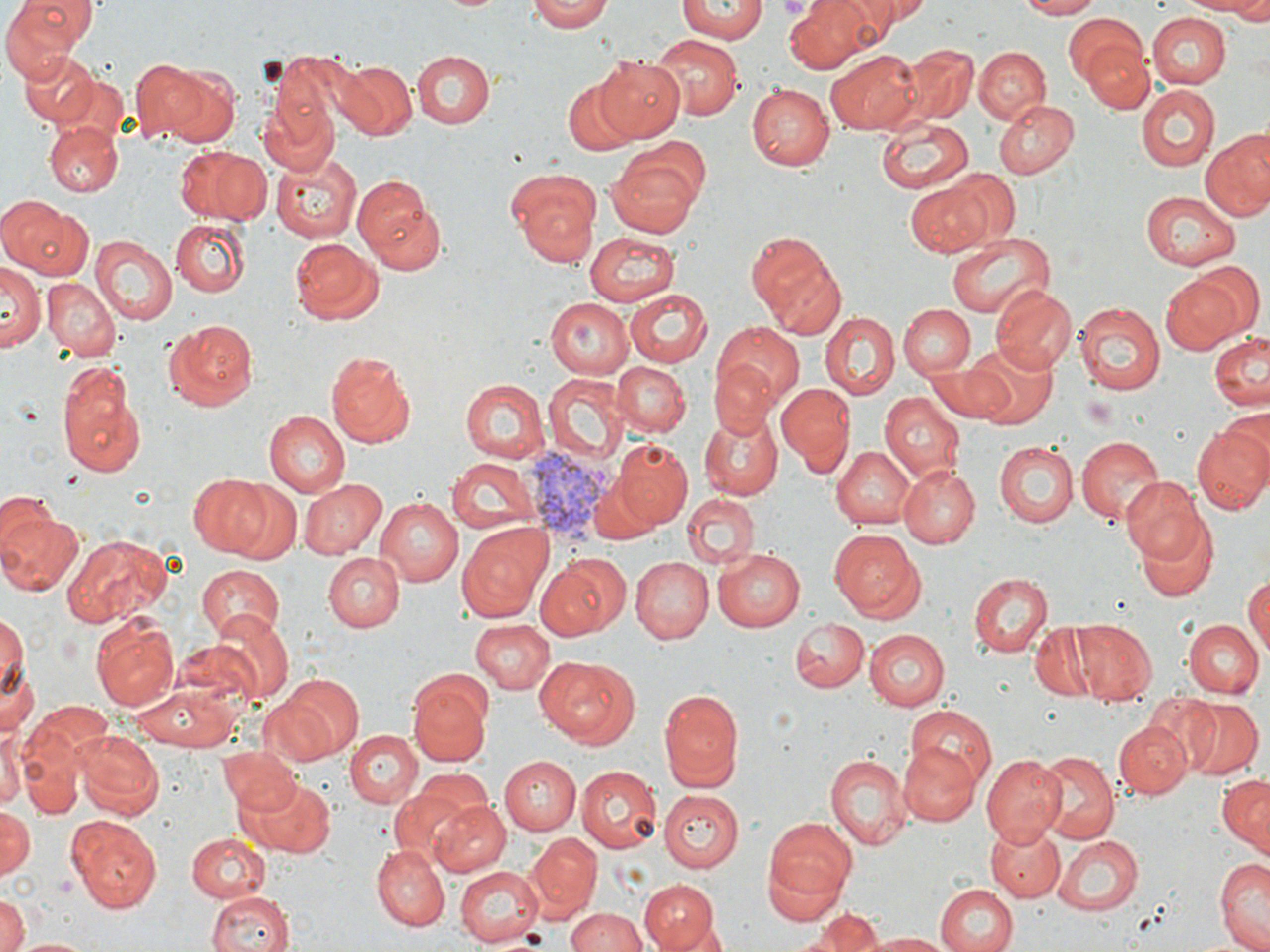

slide_level_diagnosis: Plasmodium vivax
field_of_view: single
platelet_locations: 'approximate bounding boxes as (x1, y1, x2, y2) in pixels: (1081, 397, 1118, 431)'
preparation: thin blood film
plasmodium_vivax_infected_red_blood_cell_locations: 'approximate bounding boxes as (x1, y1, x2, y2) in pixels: (524, 445, 621, 551)'
stain: May-Grünwald-Giemsa
image_size: 1270×952 pixels
modality: optical microscopy
magnification: 1000x
uninfected_red_blood_cell_locations: 'approximate bounding boxes as (x1, y1, x2, y2) in pixels: (528, 0, 614, 33), (678, 0, 766, 41), (785, 0, 880, 72), (819, 0, 916, 40), (863, 0, 935, 23), (1013, 0, 1103, 19), (1178, 0, 1270, 19), (433, 1, 511, 14), (2, 2, 94, 71), (1062, 12, 1150, 90), (1147, 13, 1228, 88), (652, 35, 743, 121), (1079, 36, 1155, 114), (896, 45, 977, 127), (975, 46, 1048, 123), (411, 50, 494, 127), (825, 50, 925, 134), (19, 52, 101, 126), (269, 52, 372, 142), (131, 56, 234, 147), (596, 57, 684, 139), (335, 60, 417, 141), (562, 78, 640, 155), (744, 83, 833, 170), (1137, 85, 1219, 170), (259, 90, 340, 177), (992, 97, 1078, 178), (874, 118, 974, 196), (47, 119, 122, 198), (1202, 129, 1270, 221), (171, 144, 271, 224), (608, 144, 708, 233), (273, 153, 365, 241), (506, 166, 603, 264), (939, 168, 1020, 246), (351, 173, 446, 276), (906, 182, 992, 258), (1138, 191, 1241, 269), (0, 197, 93, 280), (170, 218, 251, 297), (746, 230, 846, 335), (945, 231, 1055, 318), (584, 232, 679, 308), (90, 237, 177, 326), (288, 237, 384, 325), (1187, 260, 1265, 340), (2, 263, 42, 350), (1160, 275, 1245, 356), (43, 278, 119, 361), (991, 283, 1077, 372), (624, 289, 713, 367), (546, 298, 634, 379), (1073, 302, 1165, 395), (900, 305, 974, 378), (822, 312, 899, 399), (162, 317, 260, 412), (711, 320, 802, 413), (1208, 330, 1270, 415), (961, 341, 1057, 428), (326, 349, 417, 448), (56, 358, 148, 478), (708, 359, 779, 440), (614, 361, 690, 436), (920, 363, 1030, 425), (545, 375, 625, 463), (459, 379, 548, 462), (776, 381, 853, 472), (880, 393, 964, 480), (265, 411, 350, 495), (698, 413, 785, 499), (1192, 423, 1270, 519), (1077, 436, 1165, 523), (613, 439, 693, 529), (995, 441, 1078, 528), (833, 446, 917, 528), (448, 455, 541, 534), (901, 464, 979, 548), (187, 475, 275, 558), (296, 476, 387, 560), (1121, 476, 1210, 567), (216, 477, 306, 566), (682, 493, 759, 569), (375, 496, 464, 586), (0, 503, 83, 597), (1133, 516, 1219, 601), (458, 522, 553, 618), (829, 530, 926, 622), (66, 535, 169, 625), (713, 548, 805, 632), (322, 551, 402, 633), (539, 553, 631, 638), (629, 555, 714, 642), (195, 563, 286, 643), (969, 571, 1053, 659), (1244, 575, 1268, 654), (0, 609, 28, 710), (209, 610, 295, 702), (90, 617, 177, 712), (1186, 618, 1264, 696), (790, 619, 869, 691), (471, 620, 556, 693), (1072, 621, 1158, 704), (1028, 625, 1104, 700), (864, 629, 949, 711), (2, 643, 40, 745), (536, 657, 639, 750), (275, 675, 364, 760), (407, 682, 492, 768), (132, 683, 238, 748), (659, 687, 745, 791), (1148, 694, 1225, 773), (1181, 696, 1262, 778), (24, 701, 116, 778), (348, 705, 472, 799), (904, 705, 997, 787), (1113, 720, 1191, 799), (347, 728, 422, 805), (74, 729, 163, 819), (1, 730, 22, 815), (899, 743, 981, 826), (19, 746, 86, 820), (220, 749, 303, 820), (1034, 749, 1118, 844), (824, 752, 913, 848), (980, 754, 1065, 844), (500, 756, 581, 835), (575, 766, 662, 852), (390, 770, 493, 866), (1217, 773, 1269, 854), (246, 776, 336, 857), (659, 790, 743, 869), (428, 800, 510, 879), (0, 803, 35, 880), (66, 813, 163, 912), (762, 818, 856, 920), (985, 823, 1066, 902), (185, 832, 272, 901), (525, 834, 601, 919), (1055, 835, 1145, 915), (370, 846, 449, 929), (1215, 855, 1269, 952), (453, 866, 545, 947), (638, 880, 716, 951), (934, 882, 1017, 952), (204, 889, 296, 952), (0, 898, 28, 952), (568, 908, 649, 952), (806, 908, 891, 951), (860, 931, 952, 951), (11, 935, 103, 951)'